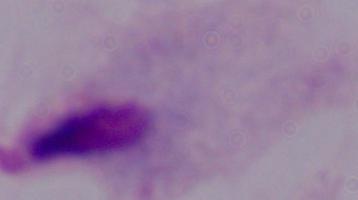
Captured at 1000x magnification. A trichomonad is seen. Micrograph.